Classify this cell by malaria status.
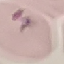

Parasitized.

Giemsa stain. Acquired by smartphone through the microscope eyepiece. Cell patch, automatically extracted from a larger field of view and resized to 64 × 64 pixels. Thin smear of blood.